Classify this cell by malaria status.
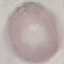
Uninfected.

Automatically extracted cell patch, resized to 64 × 64 pixels. Acquired by smartphone through the microscope eyepiece. Giemsa-stained preparation. Thin blood film.